Locate every Plasmodium falciparum-infected red blood cell.
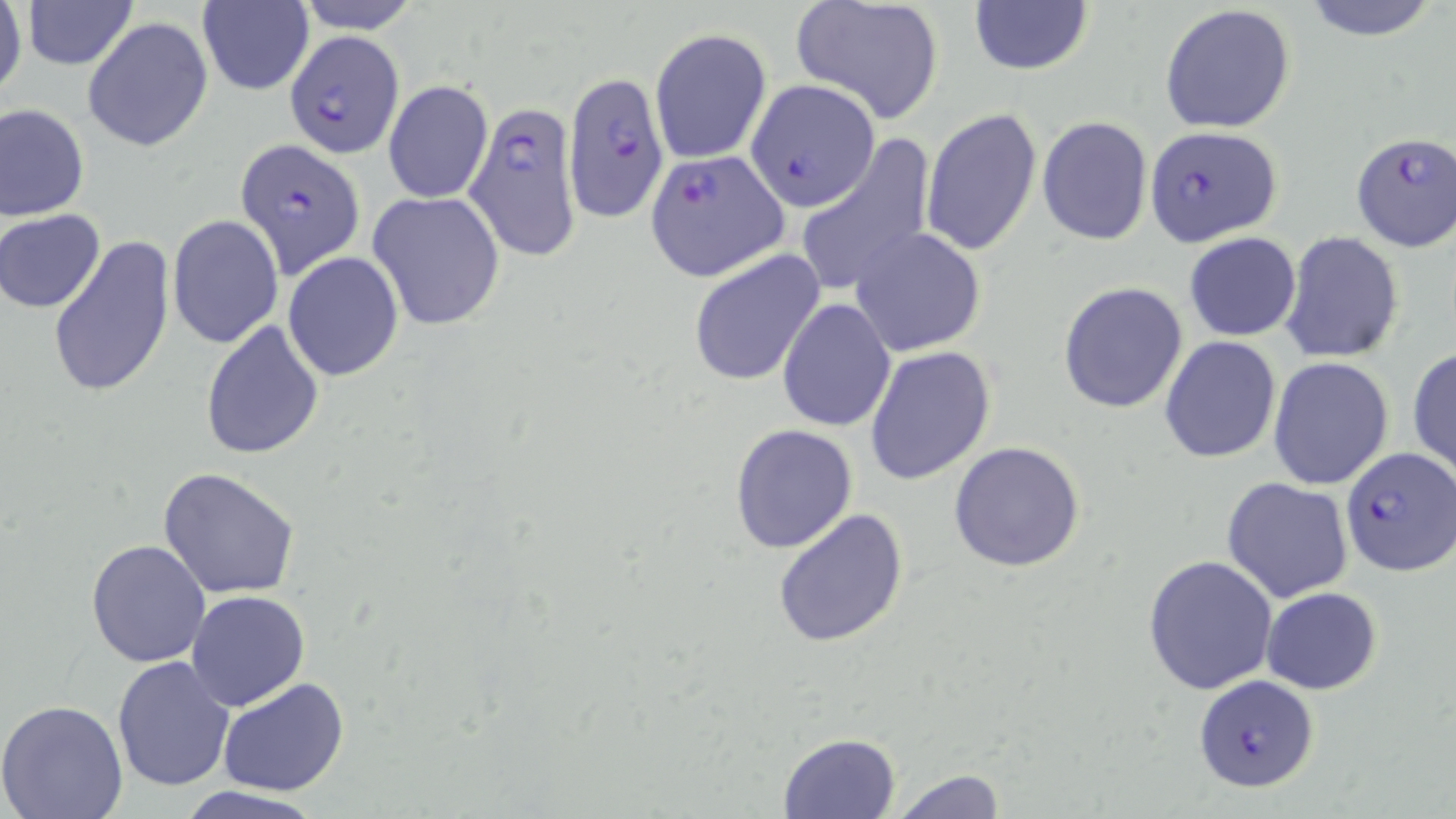
Approximate bounding boxes as named x1/y1/x2/y2 corners in pixels.
Plasmodium falciparum-infected red blood cells: (x1=286, y1=31, x2=406, y2=156), (x1=562, y1=68, x2=670, y2=225), (x1=746, y1=80, x2=881, y2=212), (x1=463, y1=100, x2=586, y2=263), (x1=1143, y1=126, x2=1282, y2=246), (x1=1351, y1=131, x2=1456, y2=251), (x1=234, y1=138, x2=366, y2=279), (x1=646, y1=150, x2=789, y2=281), (x1=1340, y1=445, x2=1455, y2=576), (x1=1194, y1=674, x2=1322, y2=793).

slide_level_diagnosis: Plasmodium falciparum
modality: light microscopy
field_of_view: single
uninfected_red_blood_cell_locations: 'approximate bounding boxes as named x1/y1/x2/y2 corners in pixels: (x1=19, y1=0, x2=140, y2=69), (x1=292, y1=0, x2=424, y2=33), (x1=790, y1=0, x2=946, y2=125), (x1=1297, y1=0, x2=1443, y2=42), (x1=1, y1=1, x2=27, y2=105), (x1=195, y1=2, x2=313, y2=96), (x1=966, y1=2, x2=1095, y2=77), (x1=1158, y1=5, x2=1297, y2=133), (x1=83, y1=16, x2=213, y2=153), (x1=650, y1=29, x2=772, y2=165), (x1=383, y1=79, x2=492, y2=204), (x1=1, y1=103, x2=90, y2=221), (x1=920, y1=106, x2=1042, y2=259), (x1=1037, y1=115, x2=1154, y2=248), (x1=795, y1=138, x2=936, y2=299), (x1=366, y1=190, x2=506, y2=331), (x1=2, y1=209, x2=105, y2=313), (x1=167, y1=214, x2=284, y2=348), (x1=850, y1=229, x2=986, y2=357), (x1=1281, y1=231, x2=1403, y2=364), (x1=1184, y1=232, x2=1302, y2=342), (x1=48, y1=233, x2=176, y2=401), (x1=688, y1=250, x2=825, y2=386), (x1=283, y1=252, x2=404, y2=382), (x1=1057, y1=282, x2=1189, y2=415), (x1=777, y1=297, x2=896, y2=433), (x1=200, y1=320, x2=326, y2=460), (x1=1159, y1=335, x2=1282, y2=464), (x1=865, y1=346, x2=996, y2=486), (x1=1408, y1=346, x2=1456, y2=482), (x1=1268, y1=358, x2=1395, y2=490), (x1=729, y1=423, x2=859, y2=554), (x1=949, y1=442, x2=1087, y2=573), (x1=157, y1=466, x2=300, y2=598), (x1=1222, y1=477, x2=1353, y2=603), (x1=771, y1=507, x2=911, y2=650), (x1=85, y1=538, x2=211, y2=668), (x1=1143, y1=552, x2=1279, y2=694), (x1=1260, y1=587, x2=1383, y2=694), (x1=186, y1=591, x2=311, y2=711), (x1=112, y1=657, x2=236, y2=791), (x1=217, y1=677, x2=349, y2=796), (x1=0, y1=700, x2=129, y2=819), (x1=776, y1=731, x2=903, y2=818), (x1=890, y1=767, x2=1007, y2=818), (x1=172, y1=786, x2=323, y2=818)'
stain: May-Grünwald-Giemsa
magnification: 1000x
preparation: thin blood film
image_size: 1456×819 pixels